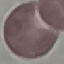
result = negative for malaria parasites
capture = smartphone camera at the microscope eyepiece
image type = cell patch, automatically extracted from a larger field of view and resized to 64 × 64 pixels
stain = Giemsa
preparation = thin smear